State which parasite is depicted.
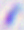
Toxoplasma gondii.

magnification = 400x
modality = micrograph